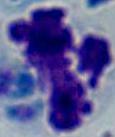
Summary:
  - Identification: white blood cell
  - Magnification: 1000x
  - Modality: photomicrograph